Look for parasitized red blood cells.
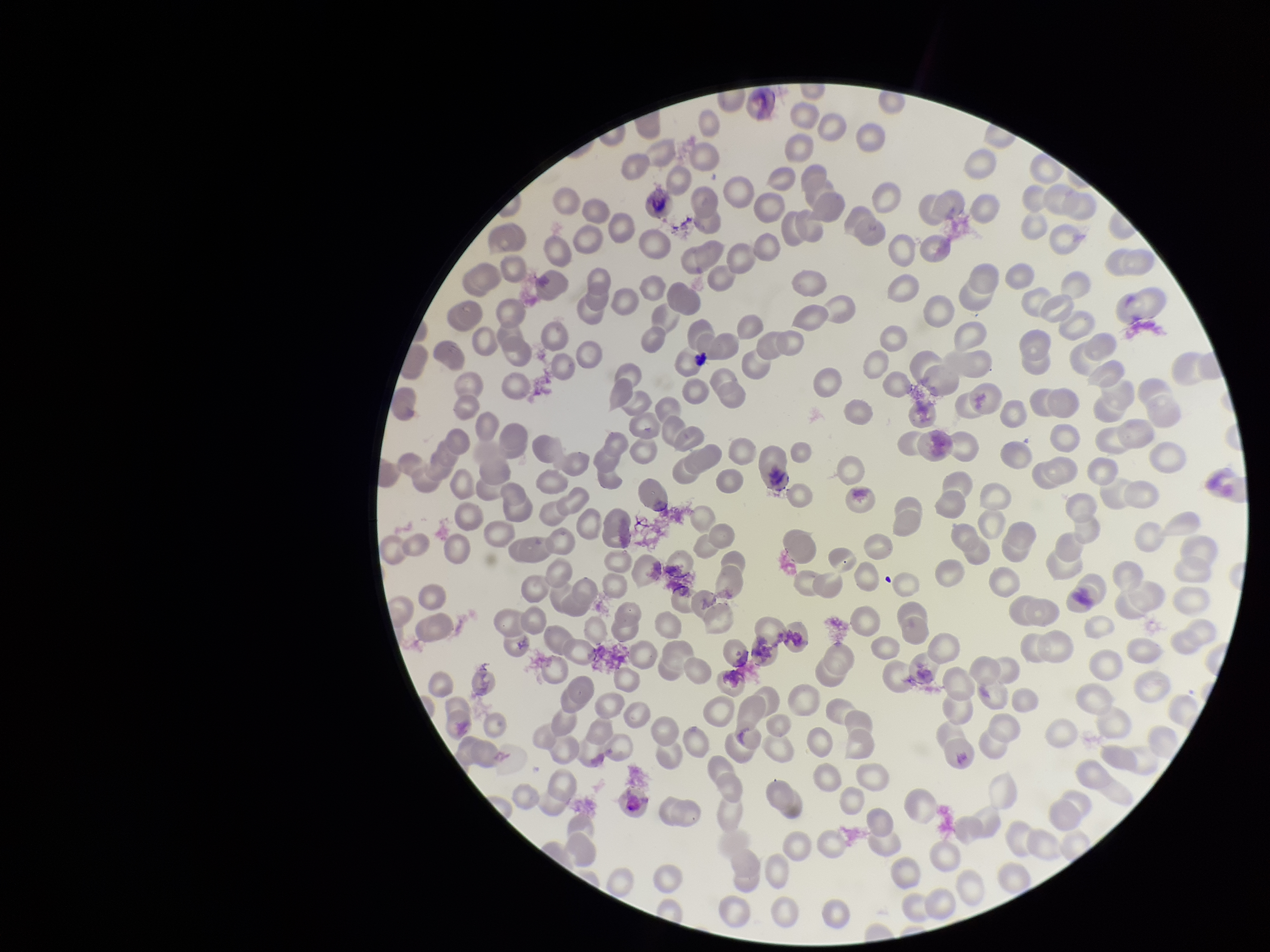

None detected.

{
  "capture": "smartphone photograph through the microscope eyepiece",
  "image_size": "1270×952 pixels",
  "parasitized_red_blood_cell_count": 0,
  "field_of_view": "single",
  "preparation": "thin smear",
  "stain": "Giemsa",
  "red_blood_cell_count": 219,
  "patient_malaria_status": "negative"
}